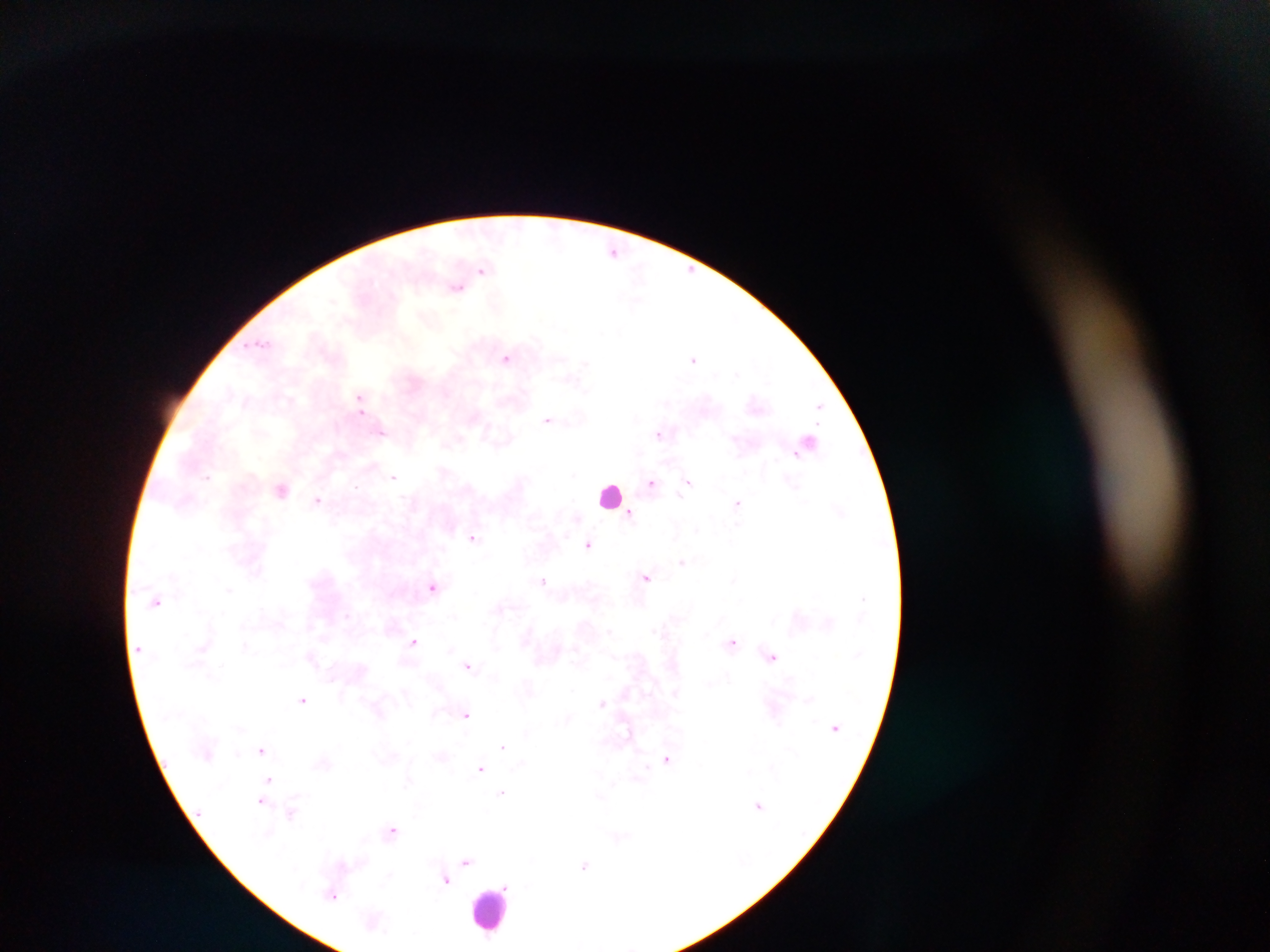

preparation: thick blood film
country: Ghana
field_of_view: single
plasmodium_parasite_locations: 'approximate centers as {x, y} in pixels: {555, 232}, {614, 251}, {690, 269}, {482, 271}, {639, 271}, {457, 288}, {636, 301}, {260, 343}, {506, 358}, {693, 359}, {584, 363}, {737, 374}, {575, 380}, {359, 397}, {819, 406}, {360, 411}, {547, 419}, {382, 432}, {659, 433}, {574, 475}, {207, 476}, {394, 477}, {651, 482}, {688, 482}, {356, 486}, {281, 490}, {679, 495}, {318, 499}, {737, 503}, {630, 513}, {697, 529}, {473, 537}, {589, 544}, {682, 561}, {646, 576}, {543, 581}, {432, 587}, {229, 589}, {157, 601}, {500, 608}, {347, 615}, {610, 631}, {413, 642}, {732, 642}, {245, 645}, {772, 656}, {468, 665}, {331, 679}, {675, 693}, {302, 699}, {809, 700}, {602, 702}, {436, 714}, {466, 715}, {569, 717}, {627, 732}, {503, 746}, {262, 749}, {441, 756}, {667, 758}, {480, 768}, {270, 779}, {408, 781}, {614, 783}, {502, 792}, {599, 796}, {262, 801}, {759, 805}, {292, 812}, {392, 830}, {619, 837}, {466, 861}, {585, 866}, {445, 879}, {506, 886}, {333, 895}'
capture: mobile-phone photograph through a microscope
leukocyte_locations: 'approximate centers as {x, y} in pixels: {609, 495}, {491, 909}'
image_size: 1270×952 pixels